Locate every leukocyte (white blood cell).
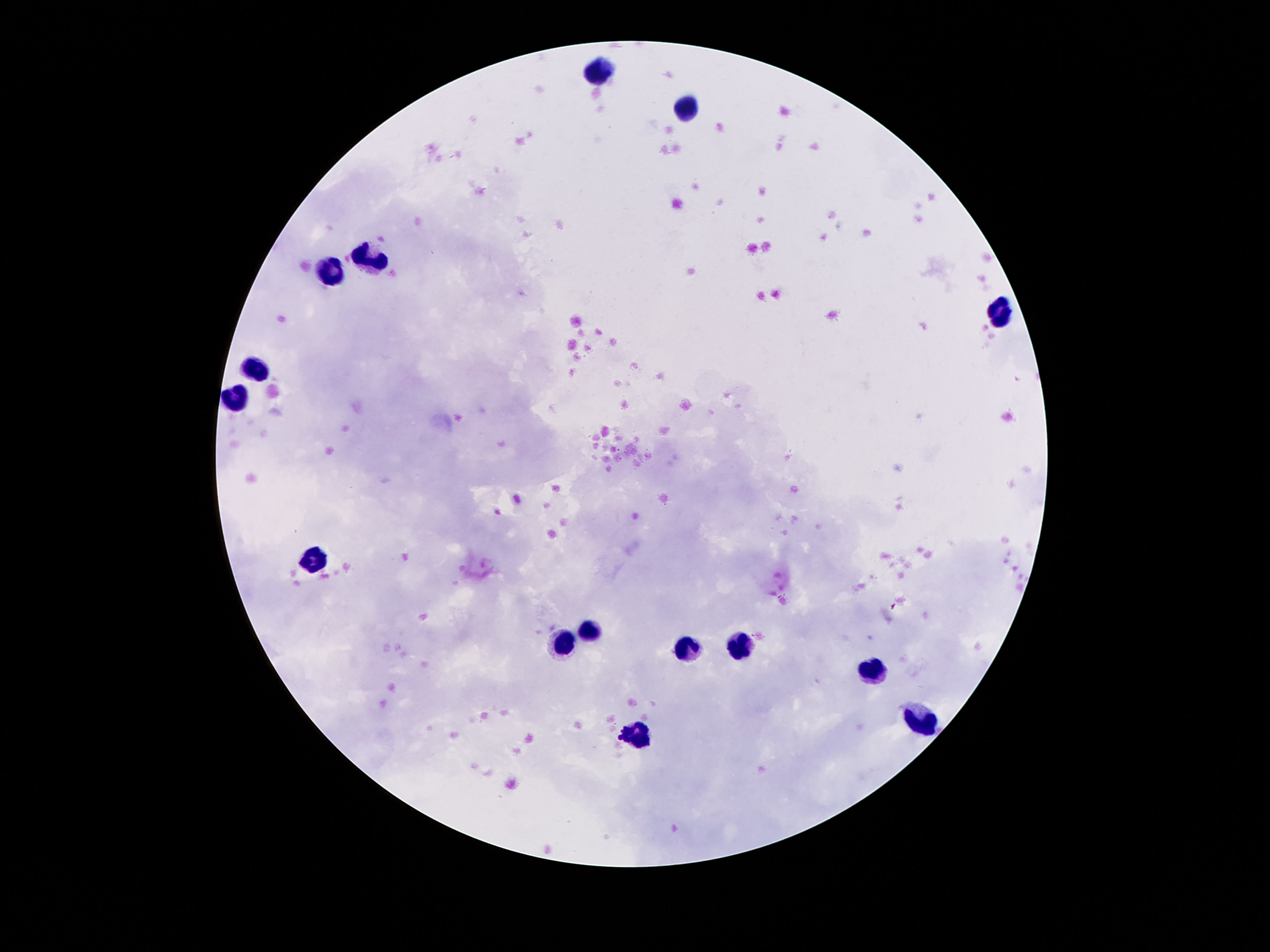
Approximate centers as [x, y] in pixels.
Leukocytes: [597, 70], [686, 111], [371, 261], [331, 276], [1000, 314], [257, 371], [236, 400], [312, 564], [589, 633], [564, 641], [740, 647], [684, 648], [872, 671], [921, 725], [639, 734].

Giemsa stain. Photographed through the microscope eyepiece with a smartphone camera. One field from this slide. 100x magnification. Image is 1270×952 pixels. Patient malaria status: negative. Thick peripheral-blood smear.